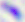
Summary:
  - Magnification: 400x
  - Identification: Toxoplasma gondii
  - Modality: micrograph